Classify this cell by malaria status.
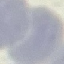

Uninfected.

stain: Giemsa
capture: smartphone through the microscope eyepiece
preparation: thin blood film
image_type: automatically extracted cell patch, resized to 64 × 64 pixels